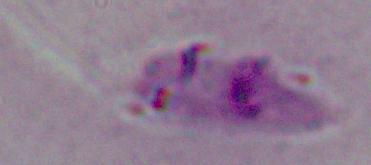 1000x magnification. Micrograph. A Leishmania parasite is shown.